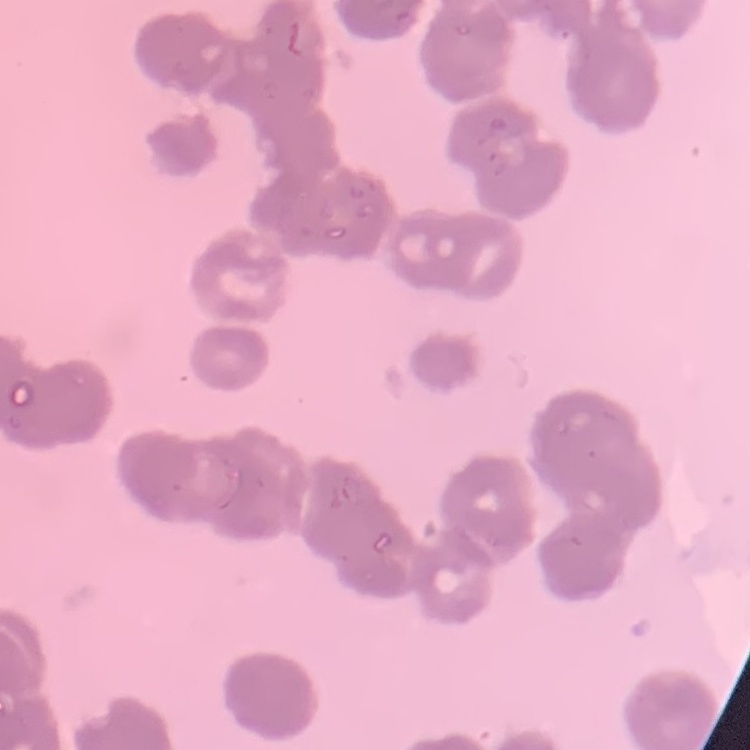
The red blood cells show rouleaux formation. Thin blood film. Field's or Giemsa stain. Square crop of a larger photomicrograph.